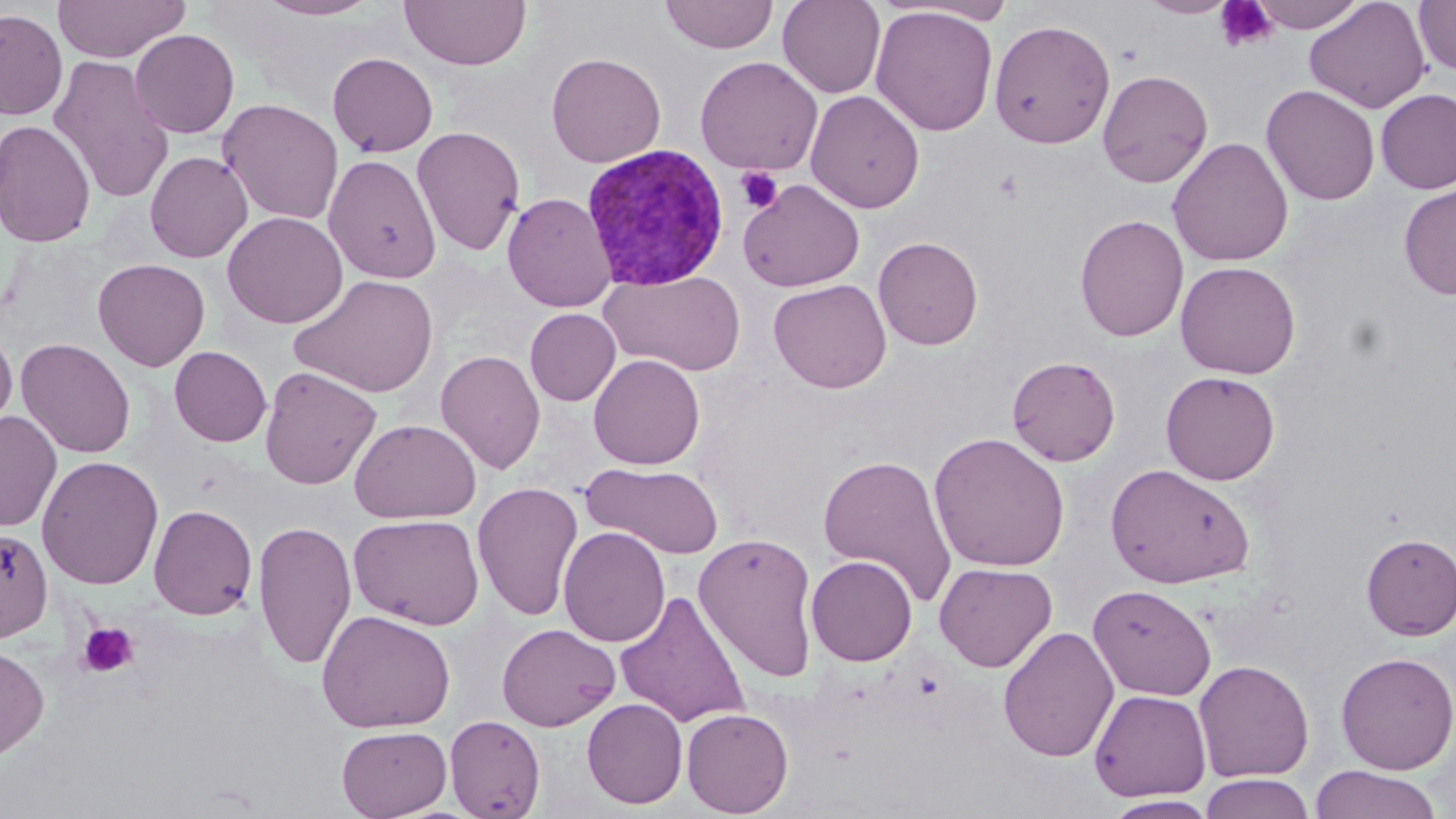
Approximate bounding boxes as [x1, y1, x2, y2] in pixels. Plasmodium vivax-infected red blood cell locations: [580, 143, 730, 291]. Uninfected red blood cell locations: [53, 0, 189, 63], [257, 0, 379, 20], [399, 0, 532, 71], [659, 0, 779, 54], [777, 0, 886, 98], [892, 0, 1020, 26], [1139, 0, 1238, 18], [1247, 0, 1367, 33], [1303, 0, 1430, 114], [1413, 0, 1456, 76], [871, 6, 998, 137], [0, 8, 68, 120], [989, 19, 1115, 149], [130, 29, 239, 138], [328, 52, 438, 157], [546, 52, 666, 168], [48, 55, 175, 204], [694, 56, 823, 175], [1097, 69, 1213, 188], [1261, 84, 1380, 206], [1375, 88, 1456, 194], [806, 90, 925, 214], [218, 97, 344, 225], [0, 119, 96, 247], [411, 126, 526, 256], [1168, 137, 1293, 267], [145, 151, 252, 262], [323, 154, 441, 282], [738, 178, 865, 292], [1398, 183, 1456, 300], [502, 192, 617, 312], [223, 211, 348, 328], [1075, 214, 1189, 342], [873, 236, 983, 350], [92, 258, 210, 371], [1174, 261, 1301, 378], [601, 270, 746, 376], [290, 273, 440, 398], [769, 279, 891, 393], [525, 308, 621, 406], [0, 323, 17, 435], [15, 337, 136, 459], [169, 346, 271, 446], [436, 349, 545, 474], [589, 354, 705, 469], [1007, 355, 1121, 466], [259, 366, 381, 489], [1160, 371, 1280, 485], [0, 411, 62, 532], [349, 418, 481, 523], [929, 432, 1070, 572], [817, 454, 957, 606], [36, 455, 164, 590], [581, 463, 723, 558], [1105, 463, 1255, 589], [472, 481, 584, 621], [148, 503, 258, 620], [349, 513, 485, 629], [253, 520, 357, 670], [558, 526, 671, 647], [0, 527, 53, 642], [694, 532, 820, 683], [1360, 533, 1456, 640], [806, 555, 917, 665], [934, 561, 1057, 672], [1088, 584, 1216, 701], [615, 589, 751, 728], [316, 609, 456, 733], [496, 623, 621, 731], [997, 626, 1119, 762], [0, 642, 51, 762], [1335, 651, 1456, 775], [1194, 659, 1314, 782], [1089, 688, 1211, 802], [582, 697, 688, 808], [681, 707, 793, 817], [445, 714, 546, 819], [336, 725, 452, 818], [1310, 765, 1442, 819], [1200, 773, 1313, 819], [1103, 795, 1220, 818]. Platelet locations: [1214, 1, 1279, 53], [736, 167, 783, 214], [77, 622, 140, 678]. Slide-level diagnosis: Plasmodium vivax. Image is 1456×819 pixels. May-Grünwald-Giemsa-stained preparation. Single field of view. Thin blood film. 1000x magnification. Optical microscopy.